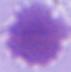
modality: photomicrograph
identification: erythrocyte
magnification: 1000x